Locate every Plasmodium parasite.
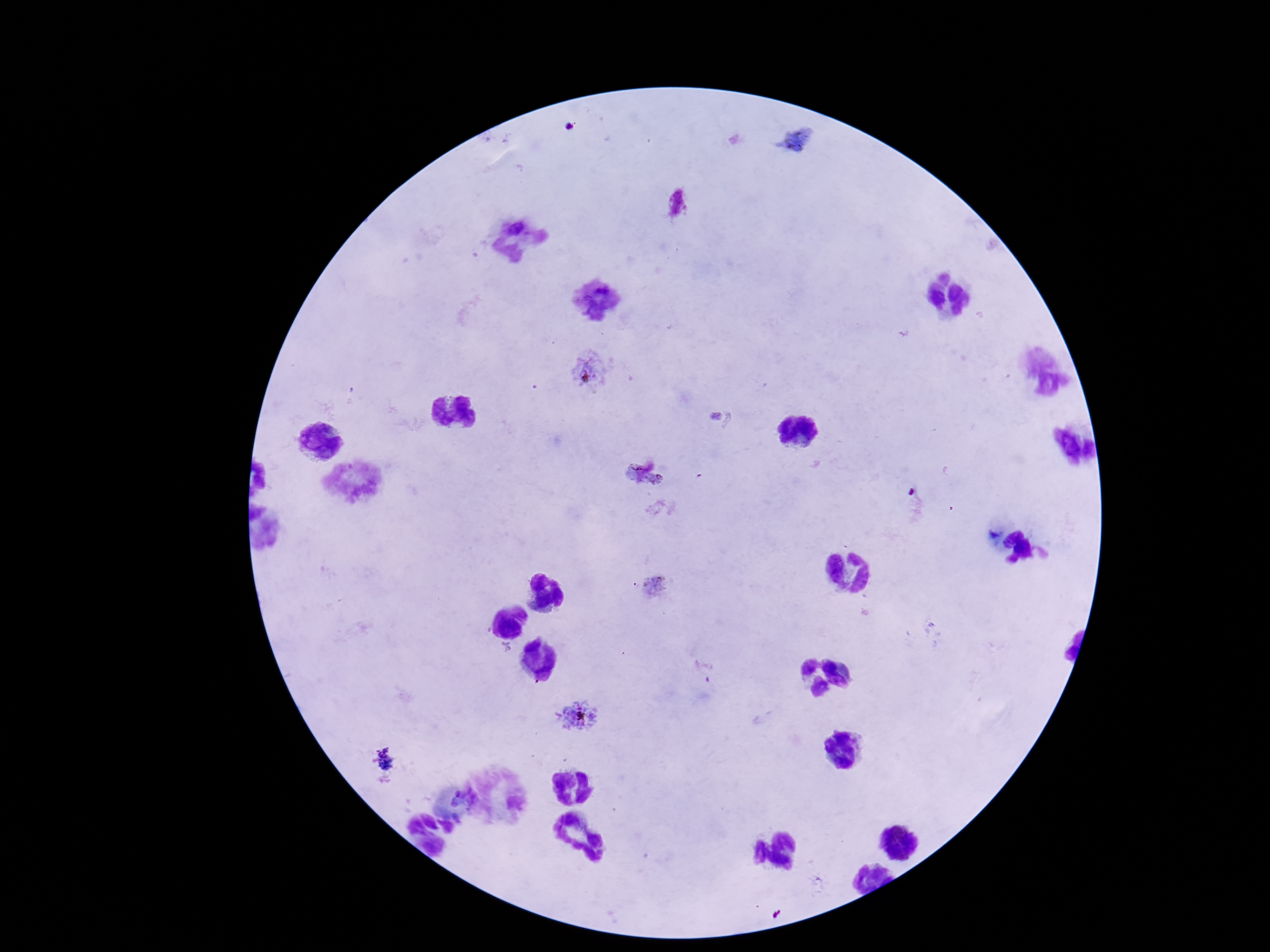

Approximate object centers, in pixels from the top-left corner.
Plasmodium parasites: (x=679, y=204), (x=588, y=370), (x=645, y=477), (x=657, y=589), (x=577, y=717).

{
  "image_size": "1270×952 pixels",
  "preparation": "thick peripheral-blood smear",
  "capture": "smartphone camera through the microscope eyepiece",
  "patient_malaria_status": "infected",
  "magnification": "100x",
  "field_of_view": "one from this slide",
  "stain": "Giemsa"
}